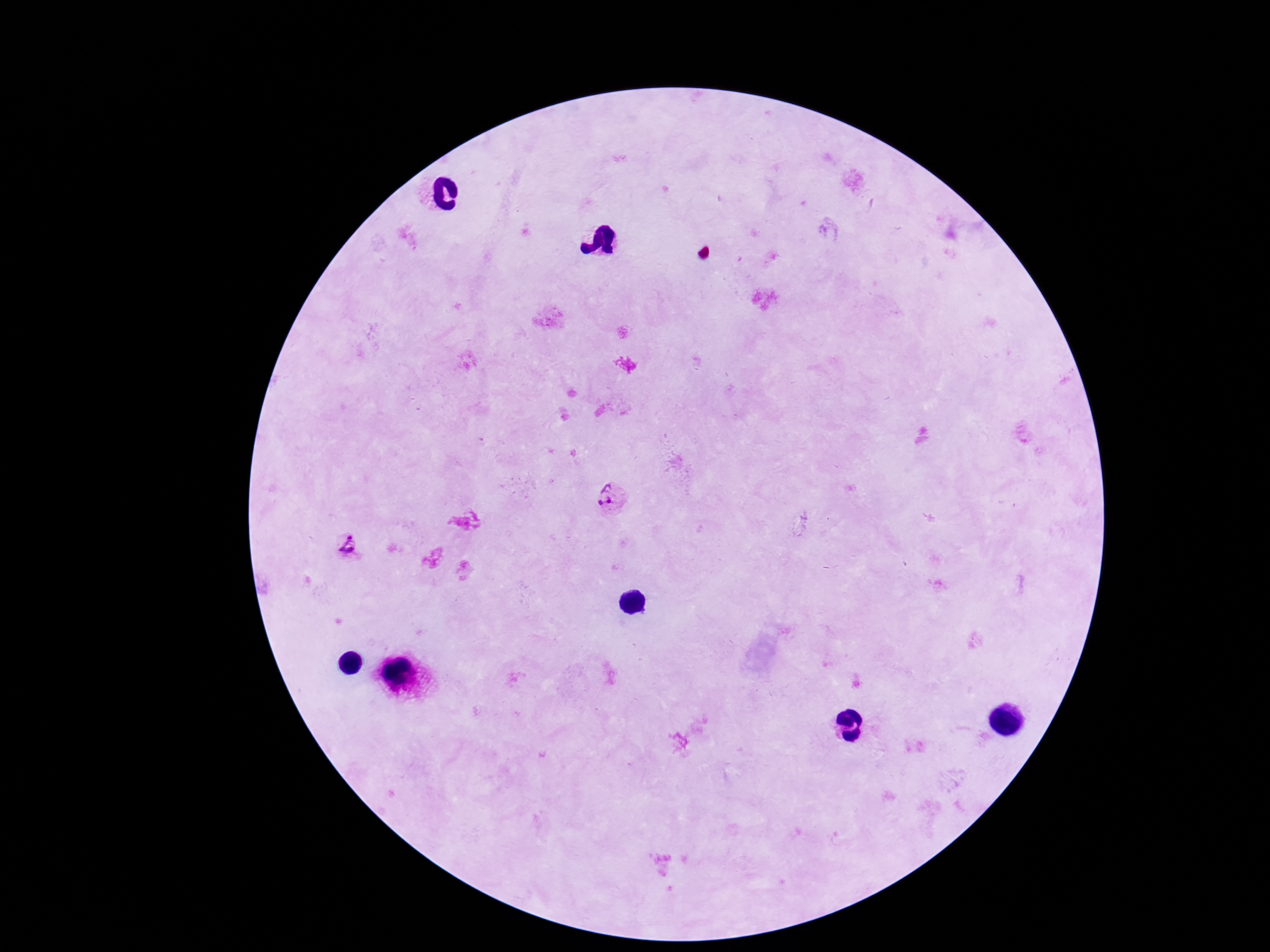 Approximate centers as (x, y) in pixels. Plasmodium parasite locations: (607, 499), (347, 547). Thick blood film. Single field of view. Giemsa-stained preparation. Smartphone photograph taken through the microscope eyepiece. Image is 1270×952 pixels. 100x magnification. Patient malaria status: infected.